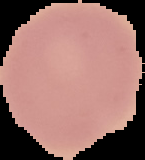

Malaria status: uninfected. Cell region segmented out of the field of view; the surrounding area is masked to black. From a thin blood smear. Image is 145×160 pixels.